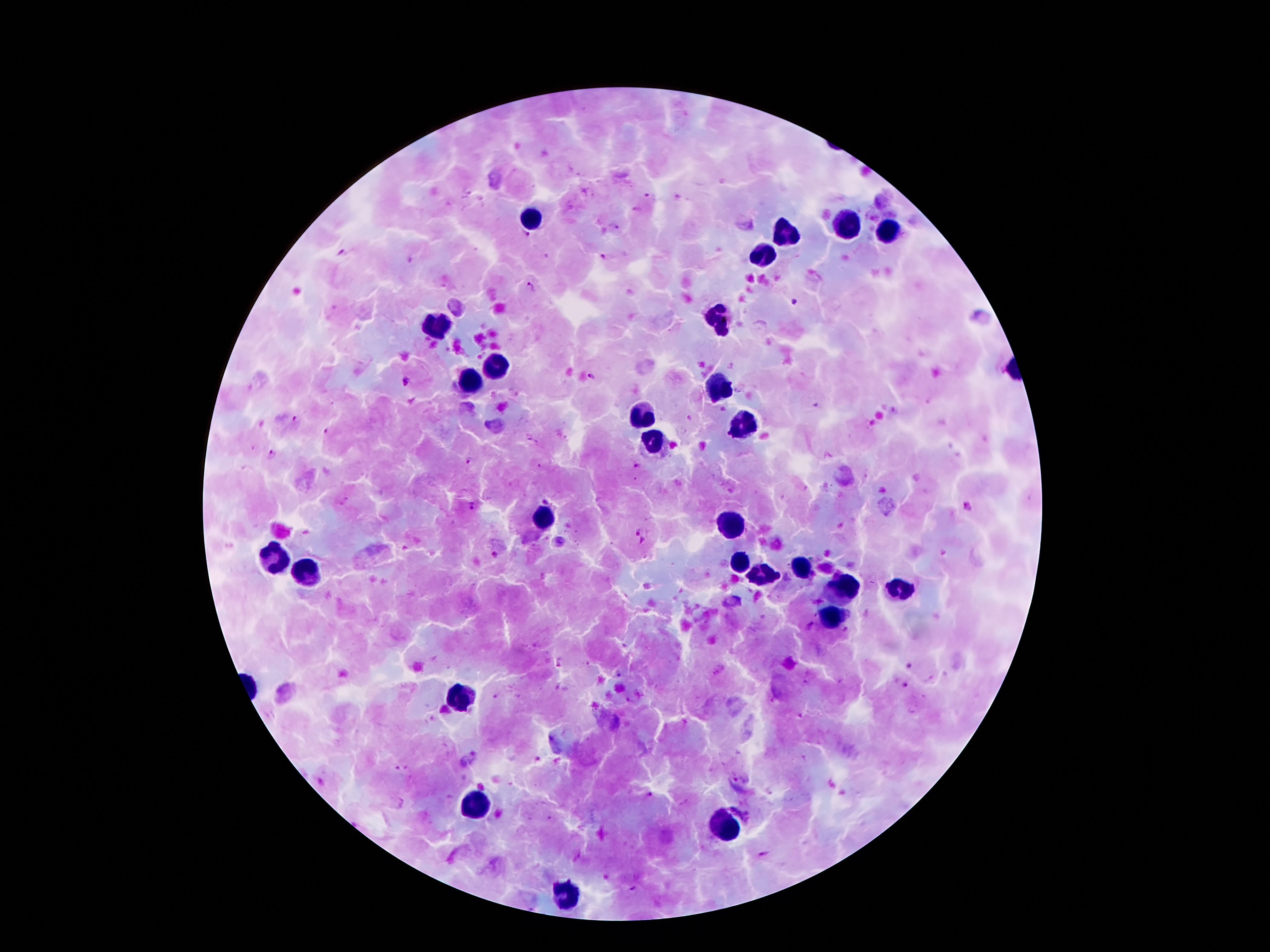

Approximate centers as [x, y] in pixels.
Summary:
  - Leukocyte locations: [530, 223], [849, 227], [885, 230], [786, 234], [763, 256], [719, 321], [439, 324], [494, 366], [472, 383], [717, 389], [645, 418], [739, 424], [659, 439], [546, 517], [729, 527], [275, 559], [741, 560], [798, 568], [304, 571], [762, 579], [842, 587], [899, 590], [832, 617], [458, 698], [474, 803], [724, 828], [565, 893]
  - Malaria parasite locations: [648, 196], [635, 208], [526, 235], [339, 251], [604, 256], [530, 287], [794, 302], [590, 376], [404, 382], [295, 420], [325, 430], [532, 442], [271, 454], [468, 461], [636, 467], [473, 506], [968, 508], [637, 532], [641, 540], [495, 555], [809, 624], [559, 663], [910, 665], [618, 675], [904, 686], [495, 694], [538, 759], [401, 769], [649, 796], [763, 855], [631, 889]
  - Patient malaria status: positive for Plasmodium falciparum
  - Preparation: thick peripheral-blood smear
  - Image size: 1270×952 pixels
  - Magnification: 100x
  - Stain: Giemsa
  - Field of view: single
  - Capture: smartphone camera through the microscope eyepiece